Assess this cell for malaria.
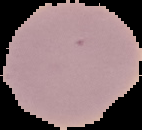

Uninfected.

preparation: thin blood film
image_type: segmented cell region with the area outside set to black
image_size: 142×130 pixels